Give a bounding box for every artifact (platelet-like body, stain precipitate, or debris).
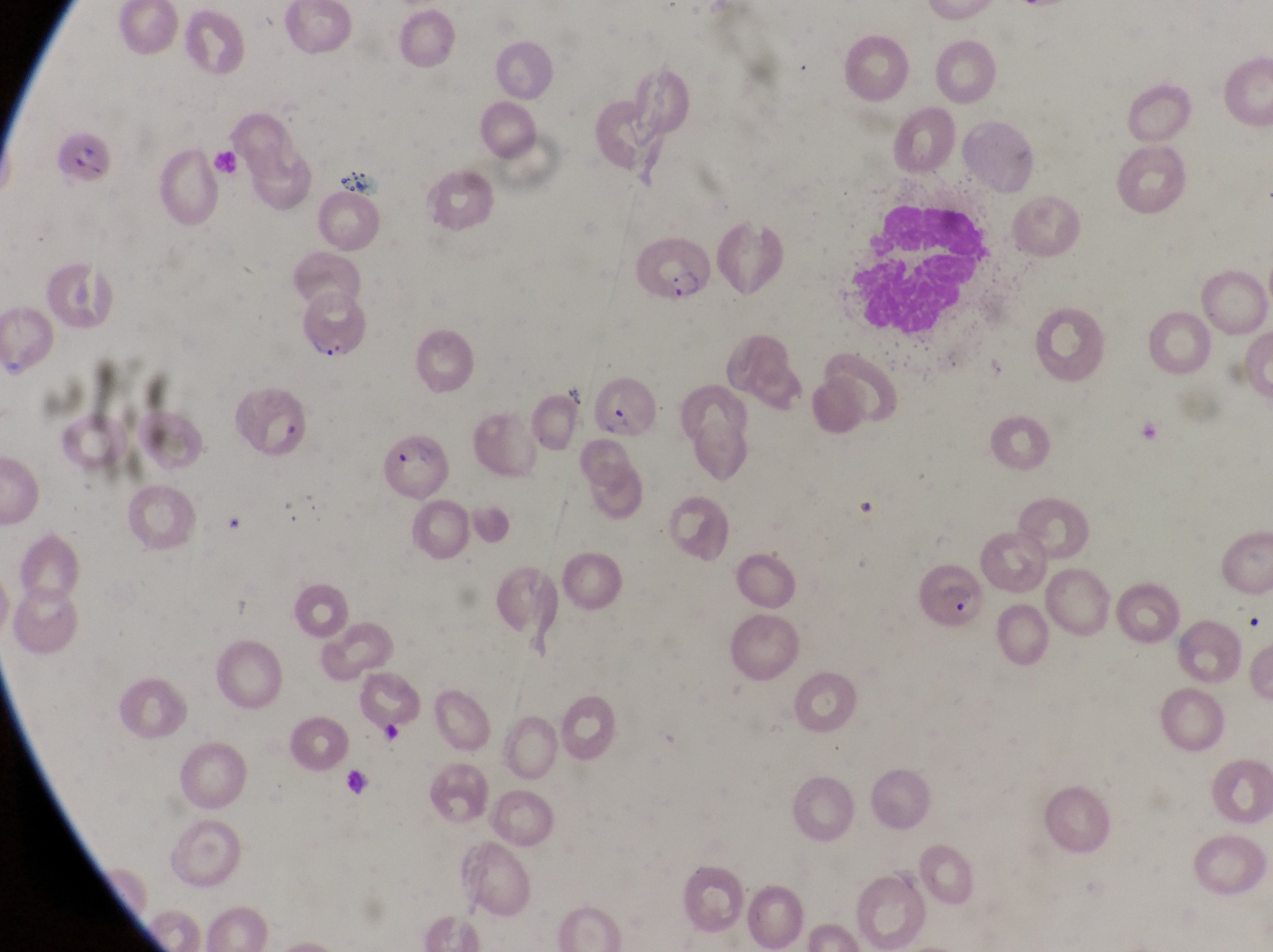

Approximate bounding boxes as {left, top, right, bottom} in pixels.
Artifacts (platelet-like body, stain precipitate, or debris): {342, 170, 383, 202}.

Summary:
  - Parasitised red blood cell locations: {52, 134, 114, 189}, {636, 234, 718, 306}, {302, 295, 369, 362}, {591, 377, 660, 437}, {232, 385, 319, 465}, {384, 434, 453, 499}, {914, 559, 988, 631}
  - Capture: smartphone photograph through the eyepiece of an Olympus CX-23 microscope
  - Image size: 1273×952 pixels
  - Preparation: thin blood film
  - Country: Uganda
  - Magnification: 1000x
  - Field of view: single